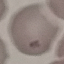 Result: no malaria parasites detected. Thin blood film. Giemsa-stained preparation. Photographed with a smartphone camera at the microscope eyepiece. Automatically extracted cell patch, resized to 64 × 64 pixels.